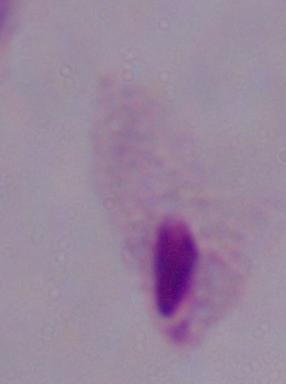
magnification = 1000x
modality = photomicrograph
identification = trichomonad